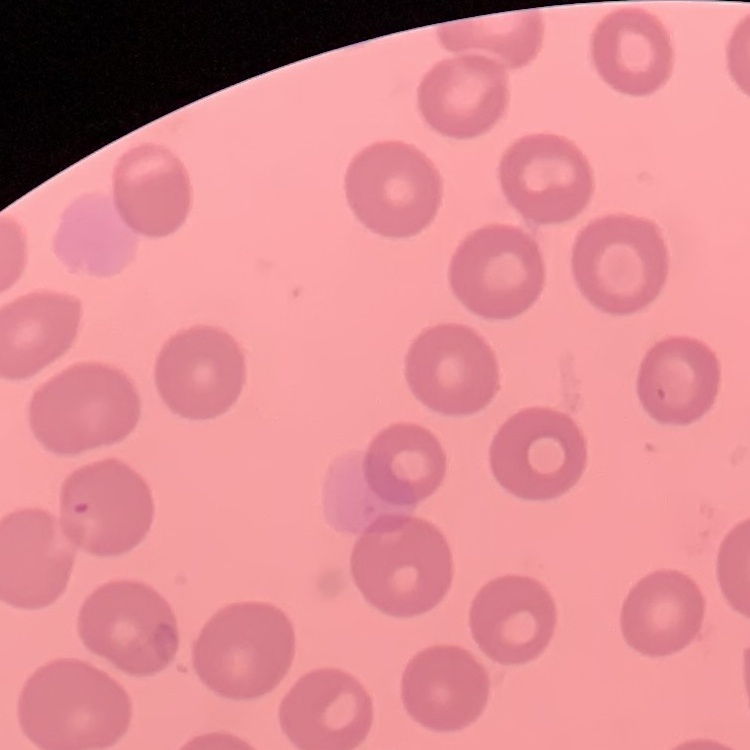
erythrocyte morphology = no rouleaux formation
image type = one tile cut from a larger photomicrograph
stain = Field's or Giemsa
preparation = thin peripheral smear